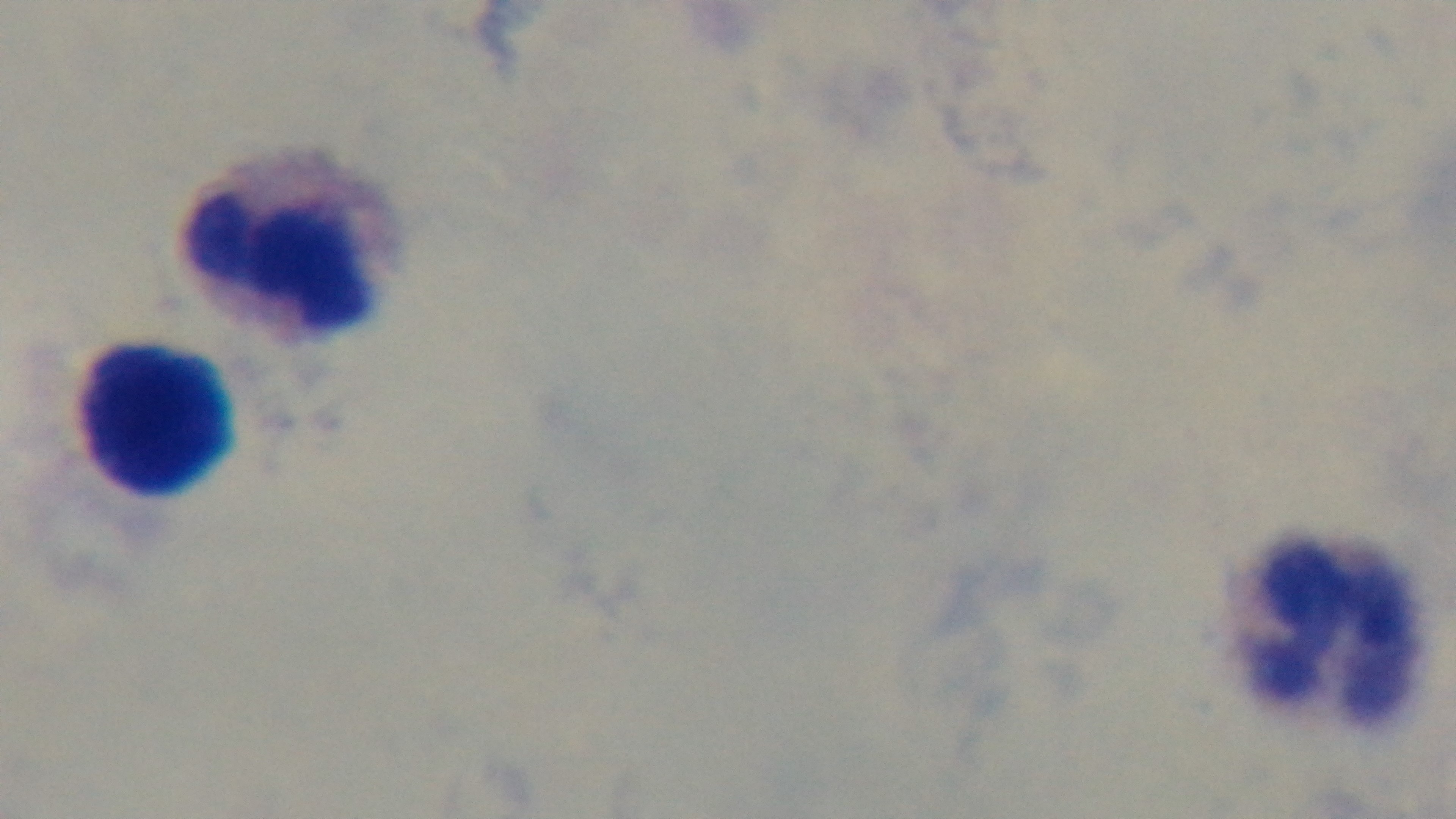

Light microscopy. Giemsa-stained. Preparation: thick. Captured with a mounted 4K digital camera. 100x oil-immersion objective. One field from the slide. Malaria status: uninfected.